Comment on the morphology of the red blood cells.
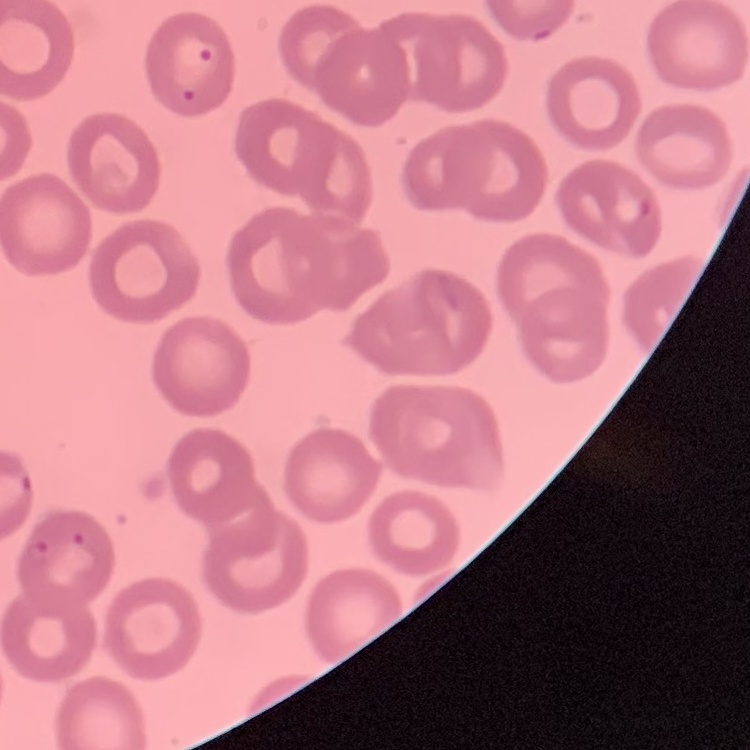

They show no rouleaux formation.

Thin blood film. Square crop of a larger photomicrograph. Stained with either Field's or Giemsa.